Report the malaria status of this cell.
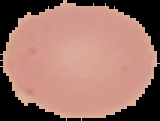

It is uninfected.

Summary:
  - Preparation: thin blood smear
  - Image size: 160×121 pixels
  - Image type: segmented cell region on a black background